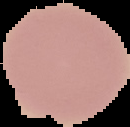

Segmented cell region on a black background. Result: negative for malaria parasites. Image is 130×127 pixels. From a thin blood smear.